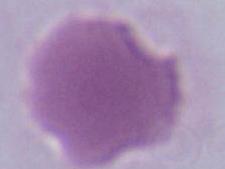

Captured at 1000x magnification. A red blood cell is shown. Micrograph.